Identify the parasite.
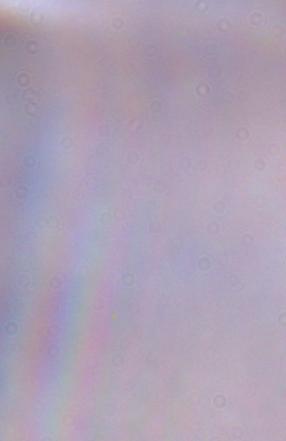

This is a trypanosome.

Summary:
  - Magnification: 1000x
  - Modality: micrograph